Comment on the morphology of the erythrocytes.
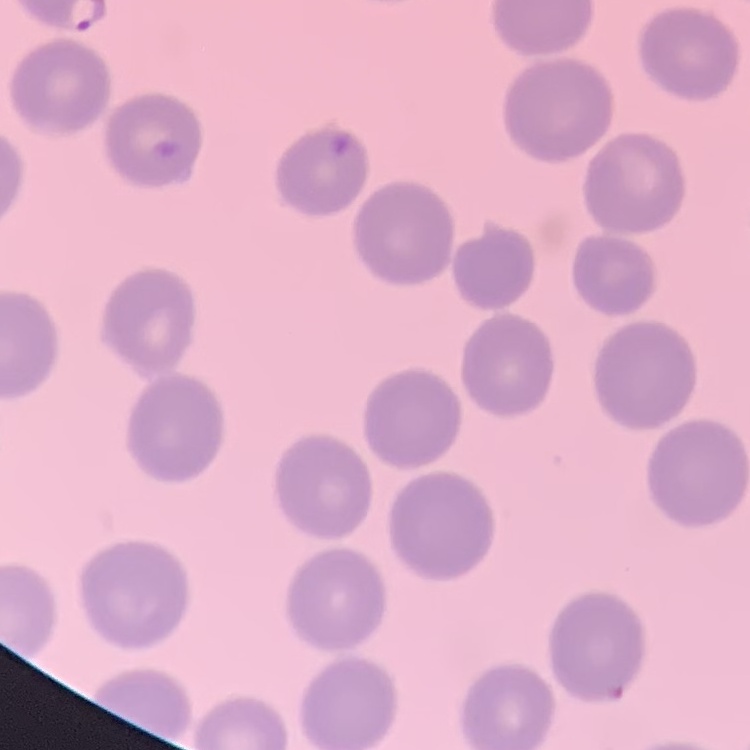

They show no rouleaux formation.

preparation = thin blood smear
image type = square crop of a larger photomicrograph
stain = Field's or Giemsa